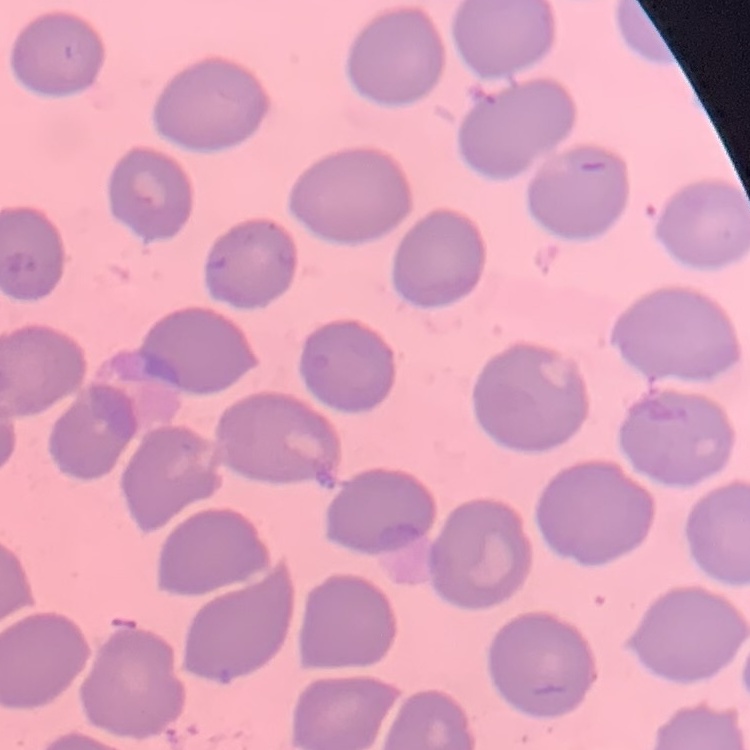

red blood cell morphology = no rouleaux formation
image type = square crop of a larger photomicrograph
stain = Field's or Giemsa
preparation = thin peripheral smear